Assess this cell for malaria.
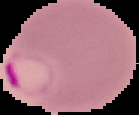
Parasitized.

Summary:
  - Image size: 139×115 pixels
  - Preparation: thin blood smear
  - Image type: segmented cell region on a black background